Report the malaria status of this cell.
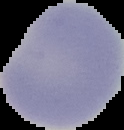
It is uninfected.

image_size: 124×130 pixels
preparation: thin blood smear
image_type: cell region segmented out of the field of view; surrounding area masked to black